Identify the blood parasite species.
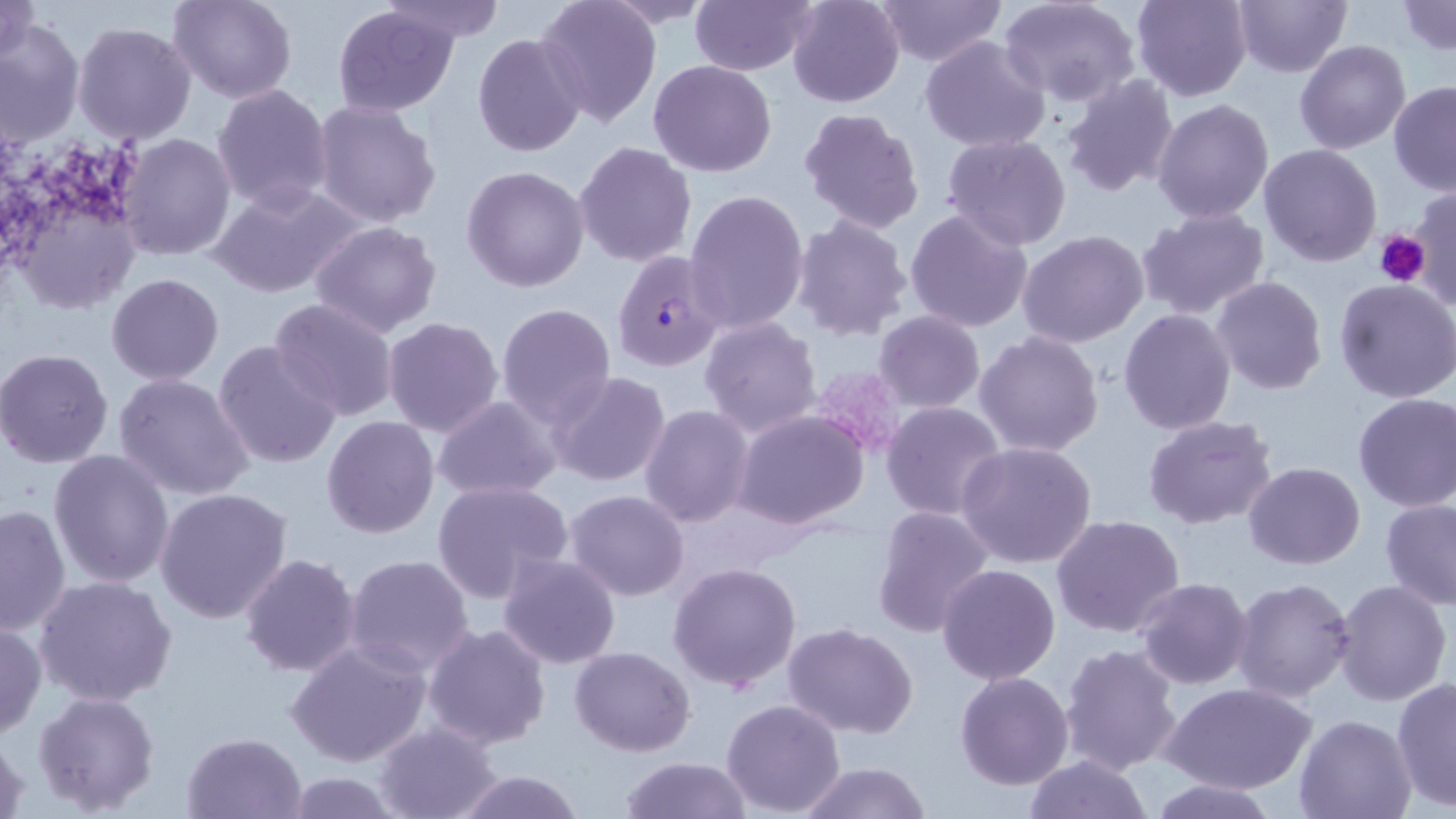
Plasmodium falciparum.

Approximate bounding boxes as named x1/y1/x2/y2 corners in pixels. Uninfected red blood cell locations: (x1=0, y1=0, x2=40, y2=70), (x1=168, y1=0, x2=296, y2=103), (x1=376, y1=0, x2=506, y2=42), (x1=604, y1=0, x2=721, y2=28), (x1=689, y1=0, x2=816, y2=77), (x1=787, y1=0, x2=905, y2=109), (x1=874, y1=0, x2=1006, y2=67), (x1=1130, y1=0, x2=1252, y2=102), (x1=1231, y1=0, x2=1350, y2=77), (x1=535, y1=1, x2=661, y2=128), (x1=1001, y1=1, x2=1142, y2=108), (x1=1396, y1=2, x2=1456, y2=54), (x1=332, y1=5, x2=459, y2=115), (x1=0, y1=19, x2=85, y2=149), (x1=72, y1=22, x2=198, y2=146), (x1=472, y1=32, x2=588, y2=158), (x1=919, y1=37, x2=1051, y2=153), (x1=1295, y1=40, x2=1410, y2=153), (x1=648, y1=59, x2=777, y2=177), (x1=1061, y1=74, x2=1181, y2=195), (x1=1389, y1=82, x2=1456, y2=196), (x1=211, y1=83, x2=335, y2=213), (x1=1151, y1=98, x2=1274, y2=224), (x1=311, y1=99, x2=442, y2=227), (x1=798, y1=108, x2=925, y2=234), (x1=118, y1=132, x2=235, y2=261), (x1=942, y1=133, x2=1072, y2=251), (x1=573, y1=141, x2=698, y2=268), (x1=1258, y1=143, x2=1382, y2=266), (x1=461, y1=165, x2=589, y2=292), (x1=209, y1=181, x2=365, y2=298), (x1=1405, y1=184, x2=1456, y2=315), (x1=684, y1=189, x2=810, y2=335), (x1=19, y1=196, x2=142, y2=311), (x1=1136, y1=207, x2=1270, y2=320), (x1=904, y1=208, x2=1036, y2=334), (x1=789, y1=214, x2=913, y2=342), (x1=309, y1=220, x2=442, y2=337), (x1=1017, y1=231, x2=1150, y2=347), (x1=106, y1=273, x2=225, y2=386), (x1=1210, y1=276, x2=1327, y2=394), (x1=1334, y1=278, x2=1456, y2=403), (x1=267, y1=297, x2=400, y2=423), (x1=495, y1=302, x2=616, y2=426), (x1=1118, y1=308, x2=1236, y2=434), (x1=872, y1=310, x2=987, y2=414), (x1=383, y1=317, x2=505, y2=438), (x1=698, y1=317, x2=823, y2=438), (x1=692, y1=322, x2=852, y2=535), (x1=974, y1=331, x2=1106, y2=458), (x1=212, y1=339, x2=342, y2=470), (x1=0, y1=349, x2=113, y2=467), (x1=545, y1=370, x2=673, y2=490), (x1=114, y1=373, x2=256, y2=502), (x1=1353, y1=392, x2=1456, y2=511), (x1=432, y1=397, x2=562, y2=500), (x1=882, y1=401, x2=1006, y2=519), (x1=639, y1=405, x2=755, y2=529), (x1=731, y1=409, x2=872, y2=532), (x1=1141, y1=414, x2=1278, y2=531), (x1=320, y1=417, x2=440, y2=538), (x1=957, y1=441, x2=1099, y2=570), (x1=48, y1=449, x2=175, y2=588), (x1=1244, y1=462, x2=1365, y2=568), (x1=431, y1=480, x2=574, y2=601), (x1=152, y1=487, x2=294, y2=625), (x1=565, y1=489, x2=691, y2=601), (x1=1380, y1=498, x2=1456, y2=610), (x1=0, y1=503, x2=71, y2=637), (x1=869, y1=506, x2=996, y2=638), (x1=1051, y1=515, x2=1186, y2=639), (x1=343, y1=553, x2=475, y2=677), (x1=239, y1=554, x2=361, y2=676), (x1=497, y1=554, x2=622, y2=671), (x1=667, y1=560, x2=803, y2=691), (x1=935, y1=564, x2=1061, y2=685), (x1=34, y1=575, x2=177, y2=709), (x1=1231, y1=577, x2=1356, y2=704), (x1=1133, y1=578, x2=1253, y2=690), (x1=1333, y1=579, x2=1451, y2=705), (x1=0, y1=617, x2=45, y2=741), (x1=783, y1=622, x2=918, y2=737), (x1=423, y1=624, x2=553, y2=751), (x1=284, y1=639, x2=432, y2=769), (x1=1059, y1=643, x2=1183, y2=775), (x1=569, y1=646, x2=696, y2=756), (x1=954, y1=670, x2=1074, y2=790), (x1=1392, y1=675, x2=1456, y2=813), (x1=1161, y1=682, x2=1318, y2=793), (x1=31, y1=691, x2=161, y2=813), (x1=720, y1=698, x2=847, y2=817), (x1=1294, y1=713, x2=1417, y2=818), (x1=373, y1=719, x2=504, y2=819), (x1=181, y1=731, x2=307, y2=819), (x1=0, y1=734, x2=30, y2=819), (x1=1023, y1=754, x2=1153, y2=818), (x1=618, y1=755, x2=755, y2=818), (x1=796, y1=761, x2=933, y2=819), (x1=451, y1=771, x2=586, y2=819), (x1=285, y1=772, x2=402, y2=817), (x1=1149, y1=778, x2=1280, y2=818). Platelet locations: (x1=1375, y1=230, x2=1429, y2=287), (x1=806, y1=365, x2=908, y2=460). Plasmodium falciparum-infected red blood cell locations: (x1=608, y1=248, x2=727, y2=372). 1000x magnification. Light microscopy. Thin blood film. May-Grünwald-Giemsa-stained preparation. Single field of view. Image is 1456×819 pixels.